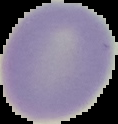
{
  "result": "no malaria parasites detected",
  "image_size": "118×124 pixels",
  "preparation": "thin blood film",
  "image_type": "segmented cell region on a black background"
}